Assess this cell for malaria.
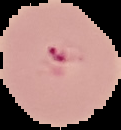

It is parasitized.

The area outside the segmented cell region is set to black. Image is 121×130 pixels. From a thin blood smear.